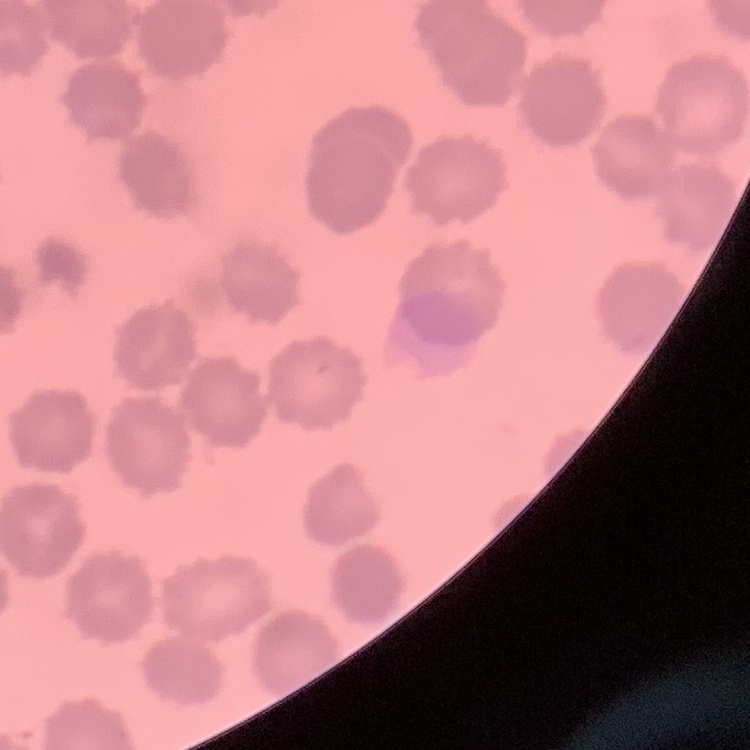

{
  "erythrocyte_morphology": "no rouleaux formation",
  "image_type": "square crop of a larger photomicrograph",
  "stain": "Field's or Giemsa",
  "preparation": "thin blood film"
}